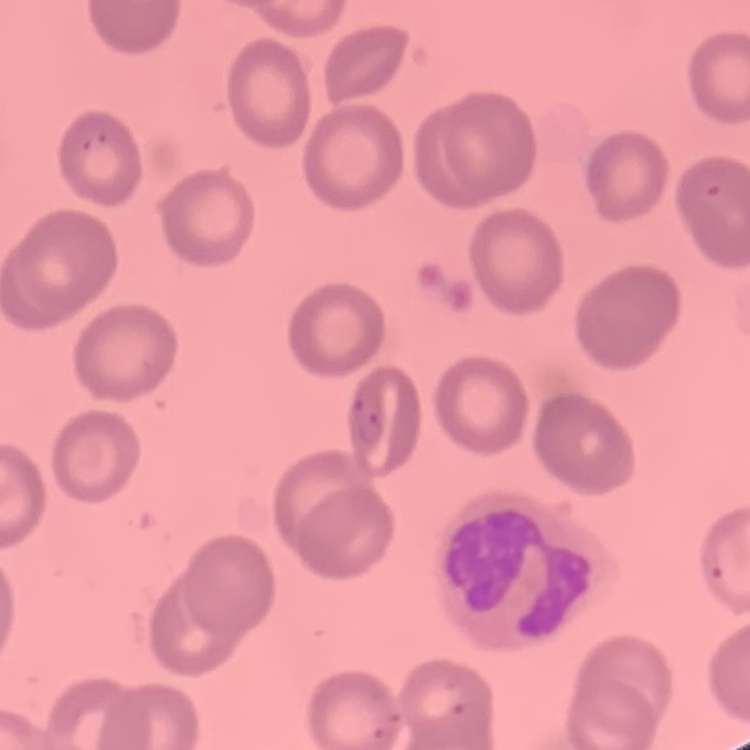
erythrocyte morphology = no rouleaux formation
image type = square crop of a larger photomicrograph
preparation = thin blood film
stain = Field's or Giemsa